Classify this cell by malaria status.
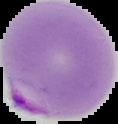
Parasitized.

Summary:
  - Image size: 118×124 pixels
  - Preparation: thin blood film
  - Image type: segmented cell region on a black background